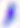 Toxoplasma gondii is seen. Micrograph. 400x magnification.